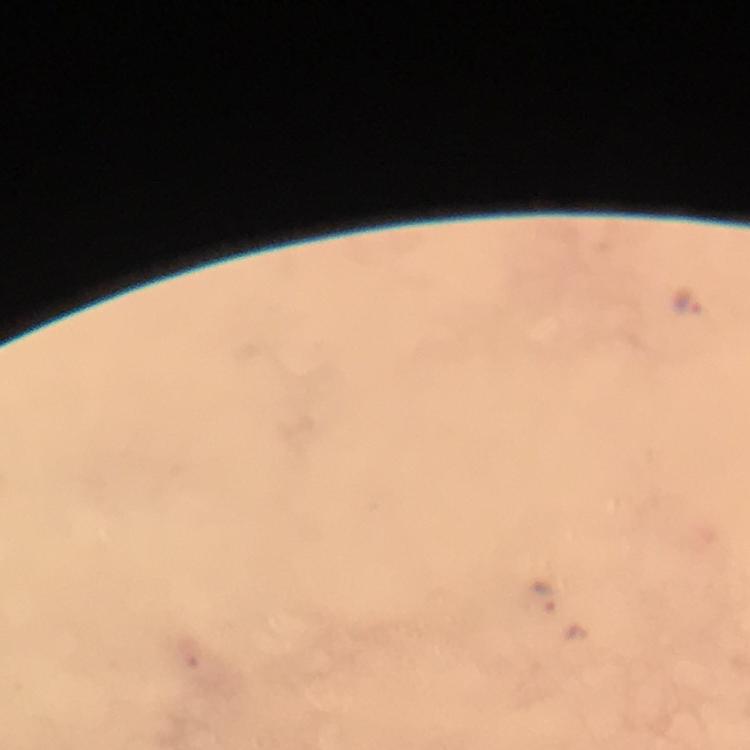

magnification = 100x
context = from a diagnostic examination for malaria
immersion oil = applied
stain = Giemsa
malaria parasite locations = approximate centers as {x, y} in pixels: {689, 299}, {543, 597}, {188, 651}
image size = 750×750 pixels
preparation = thick smear
capture = smartphone camera through the microscope
cropped from = a single field of view